Outline each blood parasite and name the species.
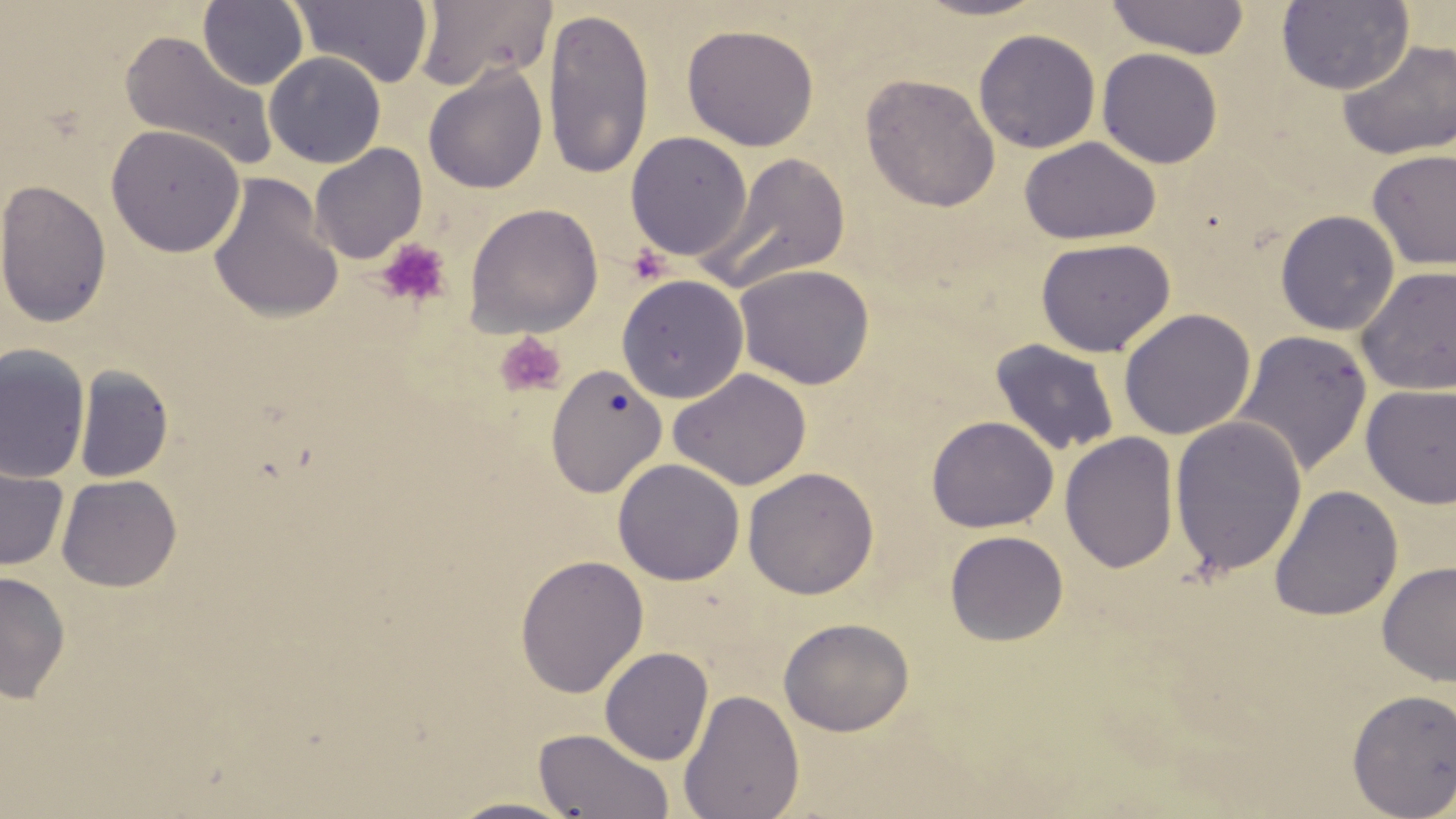

No blood parasites seen.

slide-level diagnosis = negative for blood parasites
field of view = one of a larger specimen
magnification = 1000x
uninfected red blood cell locations = approximate bounding boxes as (x1, y1, x2, y2) in pixels: (198, 0, 309, 91), (290, 0, 435, 87), (414, 0, 557, 91), (910, 0, 1052, 21), (1104, 0, 1251, 59), (1276, 1, 1414, 95), (542, 7, 655, 180), (681, 23, 819, 151), (974, 28, 1101, 154), (119, 30, 278, 172), (1337, 40, 1456, 160), (1097, 47, 1223, 169), (264, 51, 386, 168), (423, 64, 548, 194), (861, 73, 1000, 212), (106, 124, 246, 258), (624, 131, 753, 261), (1019, 136, 1161, 245), (310, 144, 427, 264), (1367, 149, 1456, 269), (705, 151, 852, 292), (207, 171, 344, 325), (1, 178, 112, 328), (463, 203, 603, 338), (1274, 209, 1400, 336), (1035, 237, 1175, 357), (734, 263, 875, 389), (1357, 265, 1456, 396), (616, 273, 749, 404), (1118, 308, 1256, 440), (1232, 330, 1373, 479), (989, 339, 1121, 457), (0, 344, 91, 484), (545, 364, 668, 498), (74, 366, 174, 483), (669, 368, 811, 490), (1361, 384, 1456, 508), (926, 415, 1059, 533), (1169, 415, 1308, 578), (1060, 432, 1180, 574), (612, 458, 745, 585), (0, 461, 69, 571), (743, 466, 879, 599), (56, 473, 182, 592), (1268, 485, 1403, 622), (945, 530, 1068, 646), (514, 553, 649, 697), (1377, 560, 1456, 686), (0, 570, 71, 703), (778, 617, 914, 736), (599, 646, 714, 765), (1346, 687, 1456, 817), (678, 688, 804, 819), (533, 727, 675, 818), (444, 797, 581, 818)
modality = light microscopy
platelet locations = approximate bounding boxes as (x1, y1, x2, y2) in pixels: (375, 238, 452, 308), (628, 244, 671, 284), (494, 331, 567, 399)
stain = May-Grünwald-Giemsa
image size = 1456×819 pixels
preparation = thin blood film